Classify this cell by malaria status.
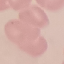

Uninfected.

capture = smartphone through the microscope eyepiece
preparation = thin blood smear
image type = cell patch, automatically extracted from a larger field of view and resized to 64 × 64 pixels
stain = Giemsa